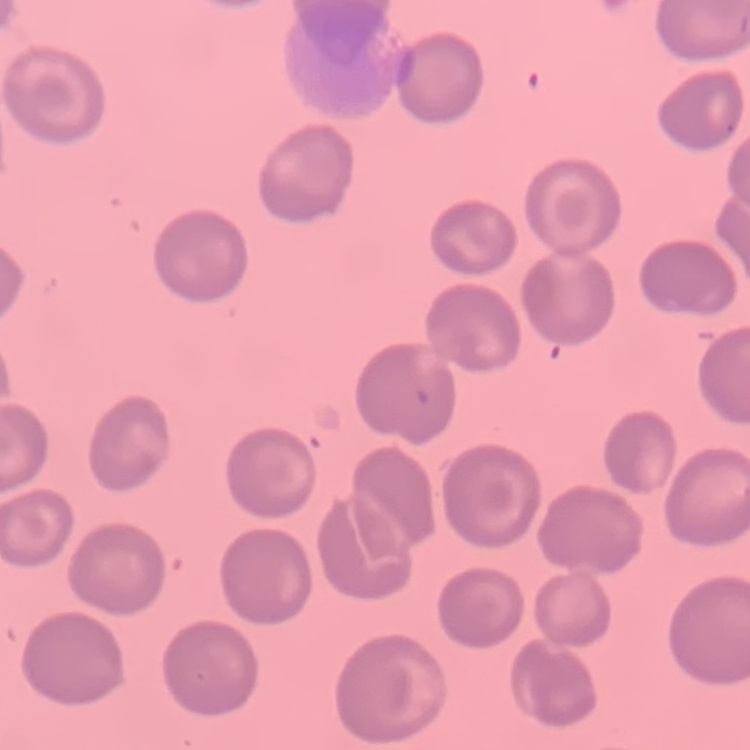
Summary:
  - Erythrocyte morphology: no rouleaux formation
  - Preparation: thin blood smear
  - Image type: square crop of a larger photomicrograph
  - Stain: Field's or Giemsa